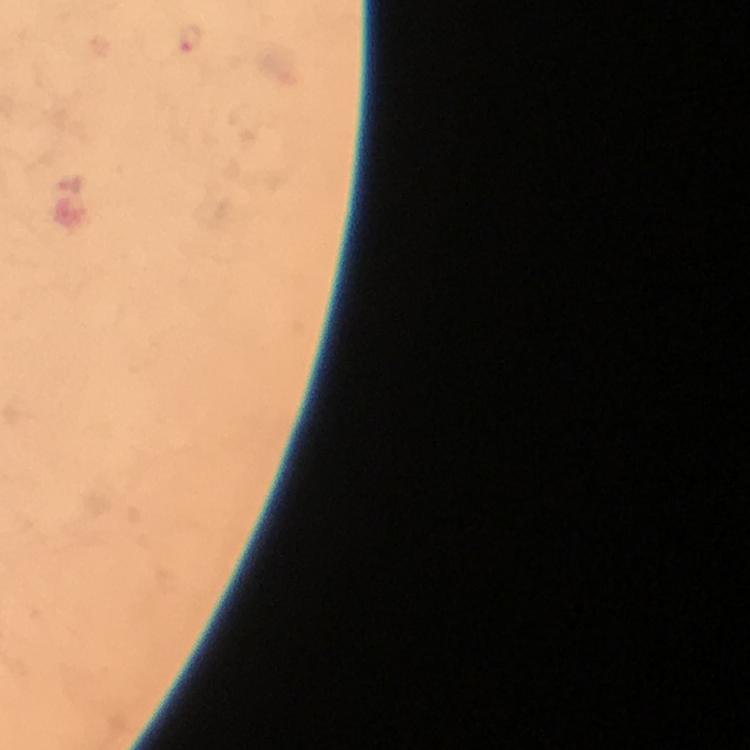
preparation: thick blood film
immersion_oil: used
malaria_parasite_locations: 'approximate object centers, in pixels from the top-left corner: (x=188, y=40)'
stain: Giemsa
cropped_from: one field of view
context: from a diagnostic examination for malaria
image_size: 750×750 pixels
magnification: 100x
capture: smartphone photograph through a microscope